Assess this cell for malaria.
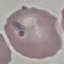
It is parasitized.

Summary:
  - Image type: automatically extracted cell patch, resized to 64 × 64 pixels
  - Capture: smartphone through the microscope eyepiece
  - Preparation: thin blood film
  - Stain: Giemsa